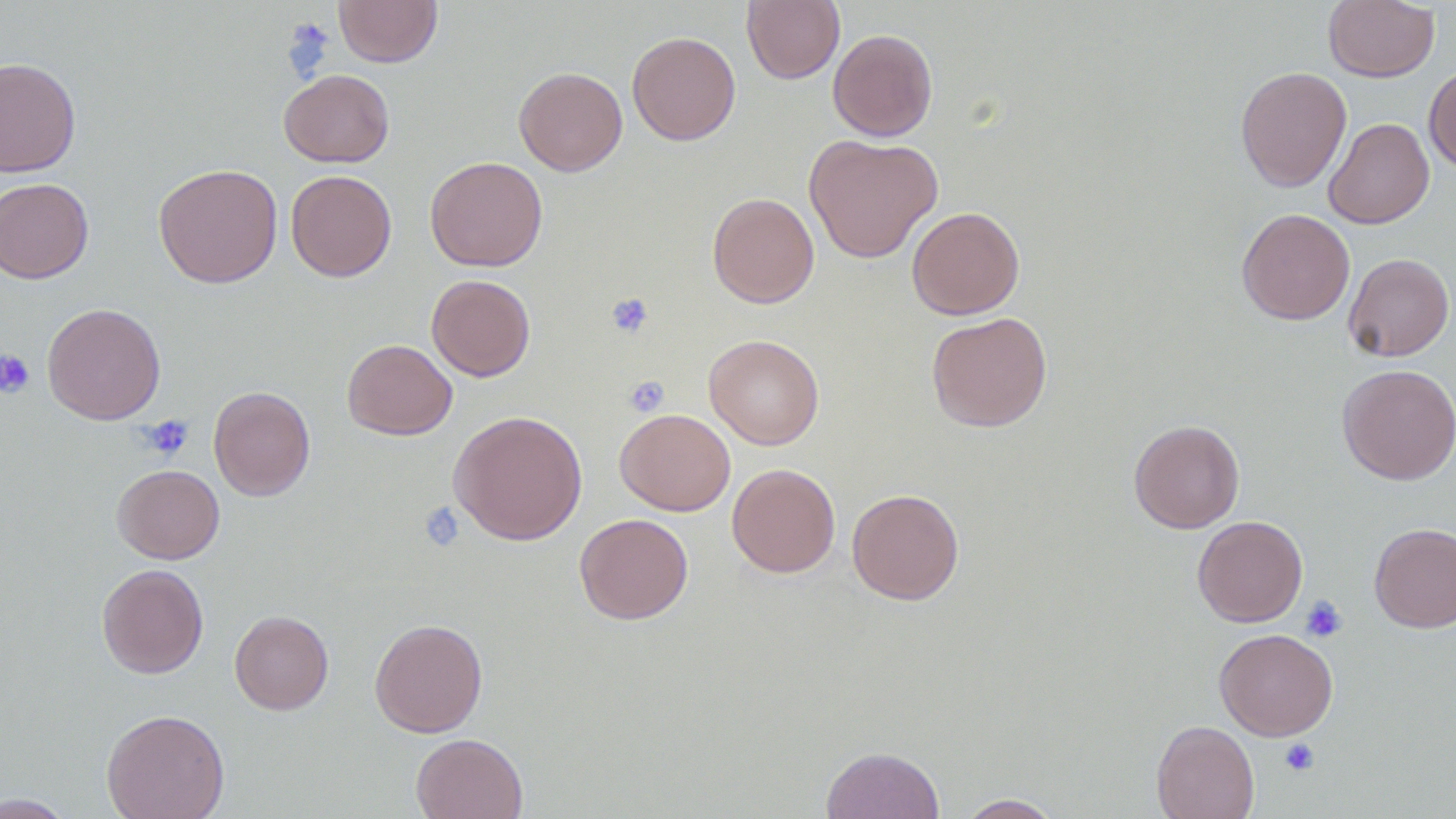
Summary:
  - Coordinate format: approximate bounding boxes as named x1/y1/x2/y2 corners in pixels
  - Uninfected red blood cell locations: (x1=333, y1=0, x2=443, y2=67), (x1=742, y1=0, x2=845, y2=85), (x1=1323, y1=1, x2=1439, y2=82), (x1=827, y1=28, x2=938, y2=142), (x1=626, y1=31, x2=741, y2=145), (x1=0, y1=57, x2=81, y2=177), (x1=1424, y1=65, x2=1456, y2=173), (x1=1235, y1=66, x2=1352, y2=192), (x1=514, y1=67, x2=627, y2=176), (x1=279, y1=69, x2=394, y2=167), (x1=1324, y1=117, x2=1434, y2=229), (x1=803, y1=134, x2=943, y2=263), (x1=425, y1=156, x2=548, y2=272), (x1=153, y1=163, x2=283, y2=289), (x1=286, y1=170, x2=397, y2=281), (x1=0, y1=177, x2=94, y2=284), (x1=707, y1=192, x2=820, y2=308), (x1=907, y1=206, x2=1025, y2=320), (x1=1236, y1=208, x2=1355, y2=325), (x1=1343, y1=253, x2=1455, y2=361), (x1=426, y1=274, x2=536, y2=382), (x1=42, y1=303, x2=166, y2=424), (x1=926, y1=312, x2=1053, y2=432), (x1=704, y1=334, x2=825, y2=449), (x1=342, y1=339, x2=457, y2=440), (x1=1338, y1=364, x2=1456, y2=485), (x1=208, y1=386, x2=315, y2=501), (x1=615, y1=408, x2=735, y2=516), (x1=448, y1=409, x2=587, y2=546), (x1=1129, y1=419, x2=1245, y2=533), (x1=726, y1=463, x2=841, y2=578), (x1=112, y1=464, x2=224, y2=564), (x1=846, y1=487, x2=964, y2=605), (x1=574, y1=513, x2=693, y2=625), (x1=1192, y1=515, x2=1308, y2=627), (x1=1369, y1=522, x2=1456, y2=633), (x1=96, y1=563, x2=209, y2=678), (x1=229, y1=610, x2=334, y2=715), (x1=369, y1=618, x2=488, y2=737), (x1=1214, y1=628, x2=1338, y2=740), (x1=101, y1=708, x2=230, y2=819), (x1=1151, y1=720, x2=1260, y2=819), (x1=410, y1=733, x2=528, y2=819), (x1=821, y1=745, x2=945, y2=819), (x1=0, y1=793, x2=77, y2=817), (x1=957, y1=794, x2=1063, y2=818)
  - Platelet locations: (x1=605, y1=292, x2=654, y2=339), (x1=0, y1=349, x2=36, y2=398), (x1=624, y1=376, x2=669, y2=417), (x1=139, y1=415, x2=194, y2=461), (x1=418, y1=502, x2=465, y2=552), (x1=1301, y1=595, x2=1348, y2=642), (x1=1280, y1=737, x2=1320, y2=777)
  - Slide-level diagnosis: negative for blood parasites
  - Magnification: 1000x
  - Preparation: thin blood smear
  - Image size: 1456×819 pixels
  - Field of view: single
  - Modality: light microscopy